State which parasite is depicted.
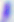
Toxoplasma gondii.

Photomicrograph. 400x magnification.